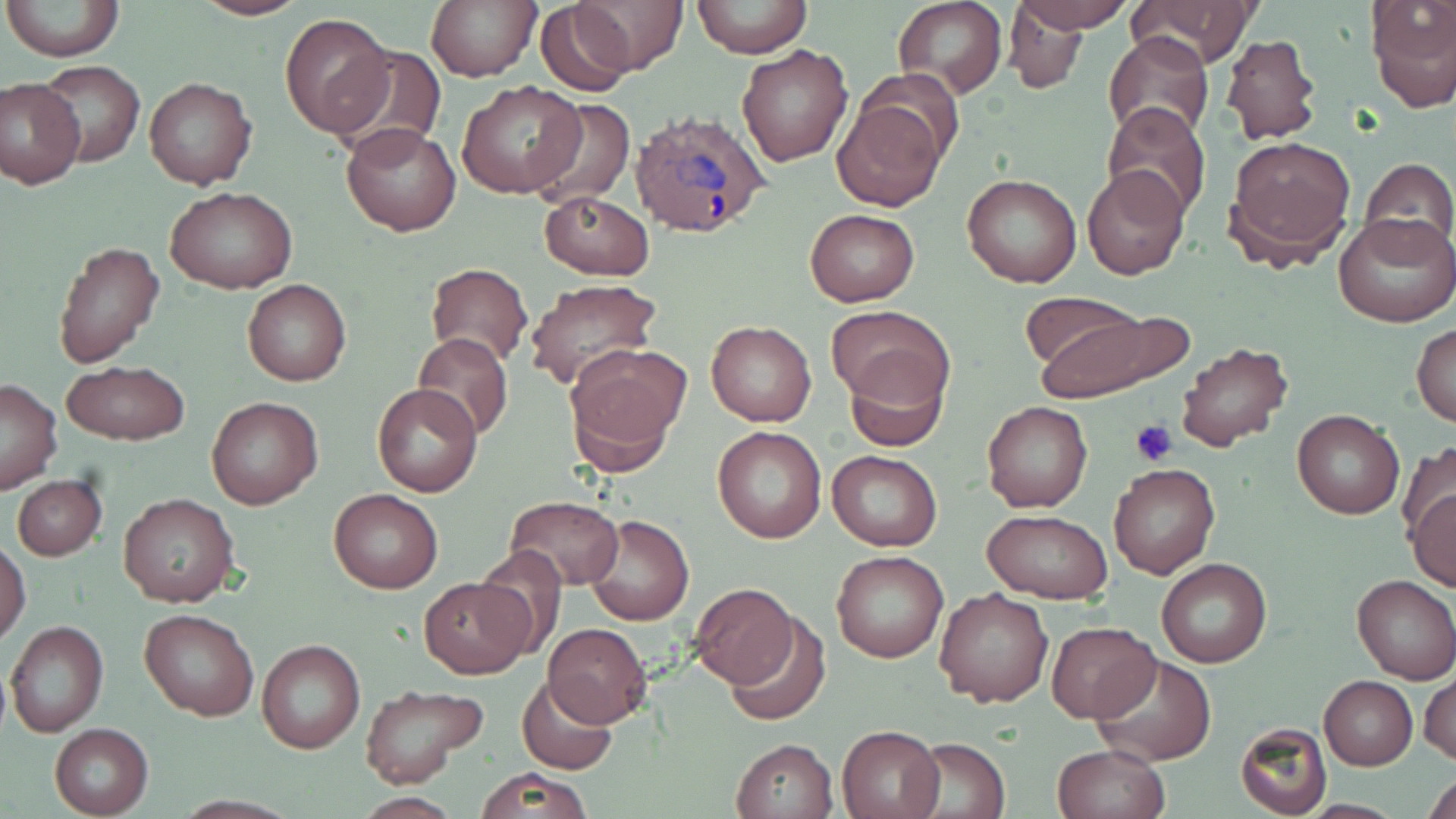

Summary:
  - Coordinate format: approximate bounding boxes as named x1/y1/x2/y2 corners in pixels
  - Platelet locations: (x1=1130, y1=418, x2=1177, y2=465)
  - Plasmodium ovale-infected red blood cell locations: (x1=631, y1=110, x2=769, y2=238)
  - Uninfected red blood cell locations: (x1=3, y1=0, x2=124, y2=65), (x1=190, y1=0, x2=312, y2=21), (x1=426, y1=0, x2=540, y2=83), (x1=571, y1=0, x2=686, y2=75), (x1=691, y1=0, x2=811, y2=60), (x1=895, y1=0, x2=1005, y2=98), (x1=1011, y1=0, x2=1134, y2=33), (x1=1133, y1=0, x2=1254, y2=69), (x1=535, y1=2, x2=636, y2=94), (x1=1366, y1=2, x2=1456, y2=114), (x1=1001, y1=5, x2=1093, y2=92), (x1=279, y1=11, x2=395, y2=139), (x1=1104, y1=32, x2=1213, y2=141), (x1=1220, y1=33, x2=1323, y2=146), (x1=332, y1=45, x2=448, y2=156), (x1=736, y1=45, x2=854, y2=166), (x1=33, y1=62, x2=146, y2=166), (x1=0, y1=76, x2=87, y2=189), (x1=144, y1=76, x2=257, y2=189), (x1=458, y1=81, x2=586, y2=199), (x1=533, y1=97, x2=633, y2=209), (x1=832, y1=97, x2=945, y2=210), (x1=1102, y1=103, x2=1212, y2=220), (x1=341, y1=122, x2=459, y2=235), (x1=1225, y1=134, x2=1356, y2=264), (x1=1358, y1=158, x2=1456, y2=257), (x1=1083, y1=166, x2=1189, y2=280), (x1=961, y1=172, x2=1083, y2=288), (x1=167, y1=187, x2=294, y2=294), (x1=536, y1=190, x2=656, y2=280), (x1=804, y1=208, x2=919, y2=306), (x1=1334, y1=212, x2=1455, y2=327), (x1=53, y1=239, x2=165, y2=368), (x1=424, y1=262, x2=533, y2=368), (x1=242, y1=278, x2=351, y2=386), (x1=523, y1=280, x2=661, y2=392), (x1=1030, y1=304, x2=1184, y2=401), (x1=827, y1=306, x2=954, y2=413), (x1=705, y1=320, x2=817, y2=426), (x1=1412, y1=324, x2=1456, y2=428), (x1=412, y1=332, x2=514, y2=442), (x1=1174, y1=342, x2=1294, y2=456), (x1=563, y1=345, x2=688, y2=474), (x1=844, y1=345, x2=951, y2=451), (x1=60, y1=362, x2=190, y2=446), (x1=0, y1=380, x2=62, y2=493), (x1=371, y1=384, x2=482, y2=497), (x1=205, y1=395, x2=324, y2=511), (x1=982, y1=400, x2=1093, y2=514), (x1=1292, y1=409, x2=1404, y2=519), (x1=712, y1=425, x2=827, y2=543), (x1=1397, y1=442, x2=1456, y2=543), (x1=826, y1=449, x2=942, y2=551), (x1=1108, y1=464, x2=1221, y2=579), (x1=12, y1=475, x2=107, y2=561), (x1=1407, y1=488, x2=1456, y2=593), (x1=329, y1=489, x2=443, y2=594), (x1=117, y1=494, x2=238, y2=608), (x1=505, y1=494, x2=625, y2=592), (x1=980, y1=509, x2=1114, y2=603), (x1=584, y1=512, x2=694, y2=626), (x1=1, y1=539, x2=31, y2=644), (x1=469, y1=545, x2=572, y2=658), (x1=831, y1=550, x2=949, y2=663), (x1=1155, y1=558, x2=1272, y2=668), (x1=1351, y1=574, x2=1456, y2=684), (x1=420, y1=577, x2=529, y2=678), (x1=687, y1=580, x2=800, y2=690), (x1=934, y1=587, x2=1054, y2=708), (x1=139, y1=608, x2=258, y2=720), (x1=724, y1=611, x2=832, y2=726), (x1=1045, y1=619, x2=1159, y2=723), (x1=5, y1=620, x2=109, y2=737), (x1=544, y1=623, x2=651, y2=726), (x1=256, y1=638, x2=365, y2=754), (x1=1089, y1=652, x2=1218, y2=765), (x1=1420, y1=671, x2=1455, y2=767), (x1=515, y1=675, x2=619, y2=775), (x1=1319, y1=676, x2=1416, y2=770), (x1=358, y1=683, x2=488, y2=788), (x1=48, y1=722, x2=153, y2=818), (x1=1235, y1=724, x2=1330, y2=818), (x1=836, y1=725, x2=945, y2=819), (x1=907, y1=736, x2=1010, y2=818), (x1=730, y1=737, x2=838, y2=818), (x1=1052, y1=744, x2=1168, y2=819), (x1=472, y1=766, x2=594, y2=818), (x1=1423, y1=770, x2=1455, y2=819)
  - Slide-level diagnosis: Plasmodium ovale
  - Preparation: thin blood smear
  - Field of view: one of a larger specimen
  - Stain: May-Grünwald-Giemsa
  - Magnification: 1000x
  - Image size: 1456×819 pixels
  - Modality: light microscopy